Give the position of every Plasmodium parasite.
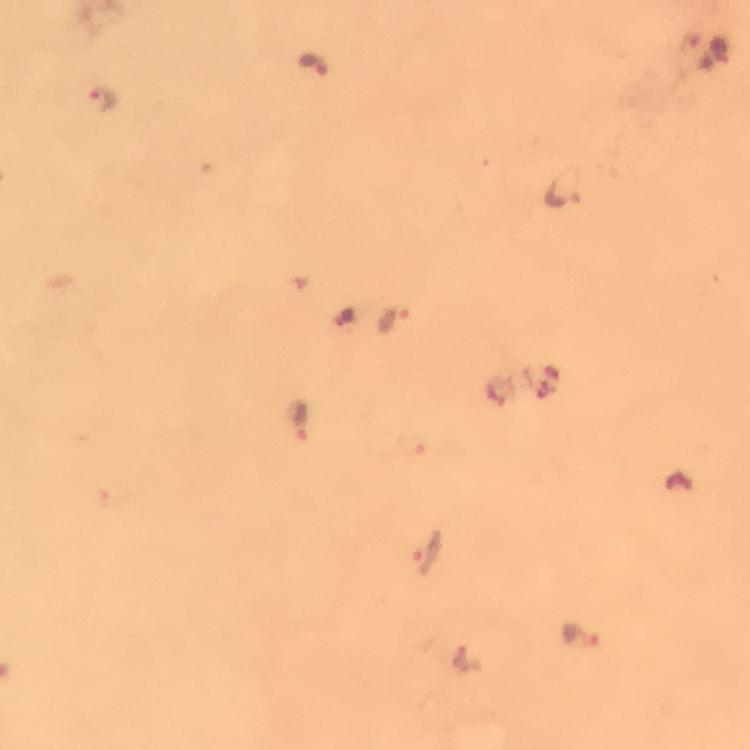
Approximate centers as (x, y) in pixels.
Plasmodium parasites: (314, 63), (103, 100), (564, 186), (395, 319), (304, 421), (408, 442), (430, 551), (580, 637), (465, 657).

image_size: 750×750 pixels
magnification: 100x
stain: Giemsa
cropped_from: one field of view
capture: smartphone mounted on the microscope
immersion_oil: used
preparation: thick blood film
context: from a malaria diagnostic workup